Identify the parasite.
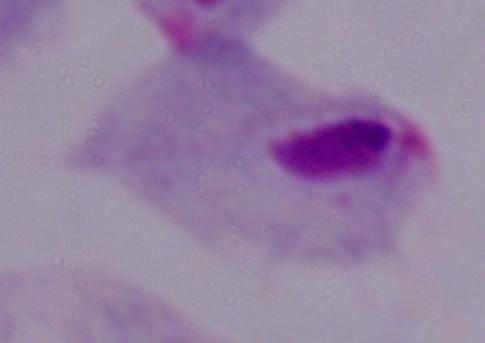

This is a trichomonad.

1000x magnification. Micrograph.